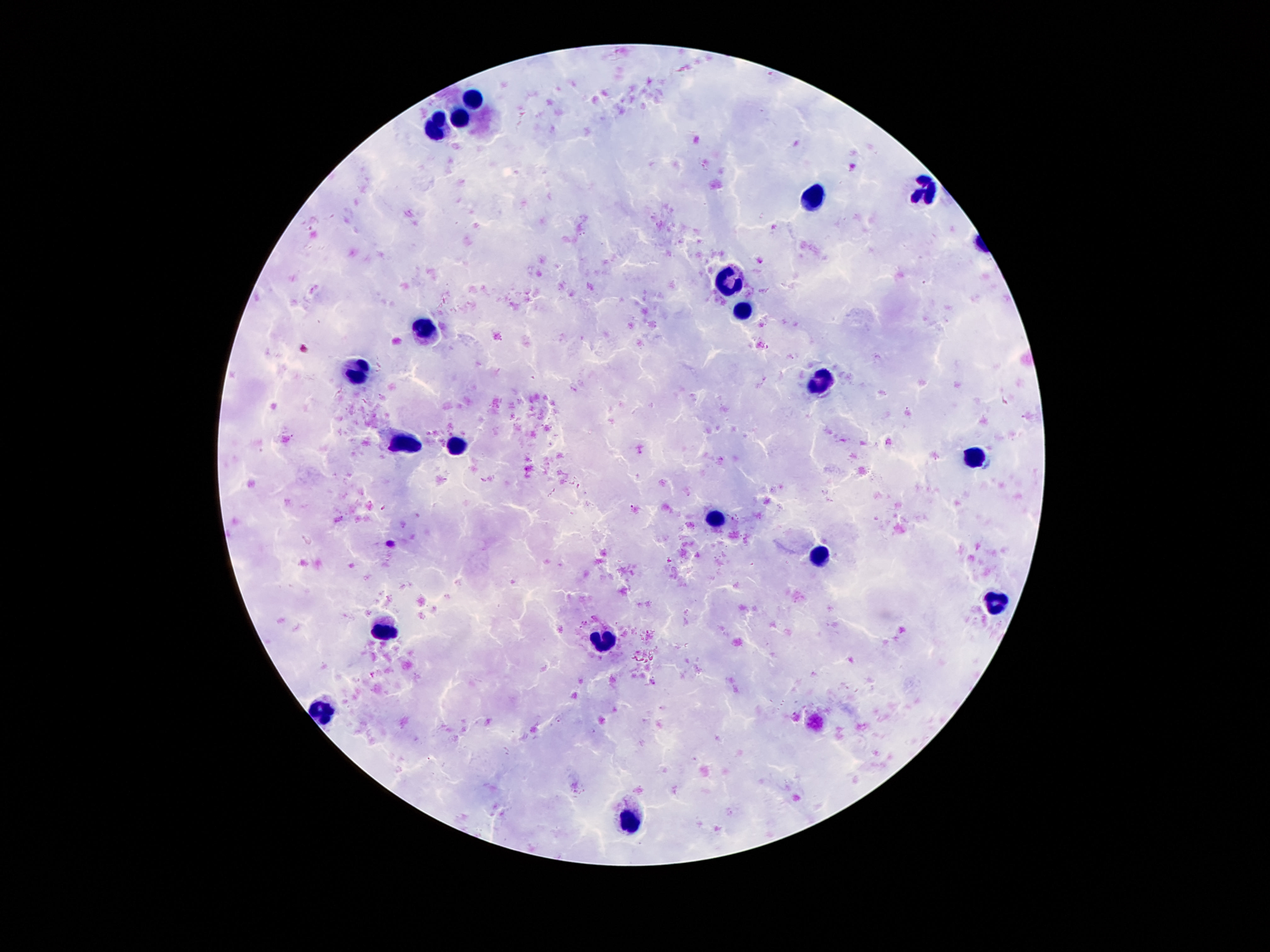
magnification: 100x
field_of_view: one from this slide
patient_malaria_status: negative
preparation: thick blood film
stain: Giemsa
capture: smartphone camera through the microscope eyepiece
image_size: 1270×952 pixels
leukocyte_locations: 'approximate centers as {x, y} in pixels: {470, 96}, {461, 119}, {439, 128}, {925, 189}, {812, 199}, {730, 277}, {740, 306}, {424, 328}, {351, 372}, {820, 381}, {406, 445}, {456, 448}, {971, 459}, {716, 519}, {823, 559}, {994, 604}, {994, 605}, {386, 629}, {606, 638}, {325, 711}, {630, 824}'